Classify this cell by malaria status.
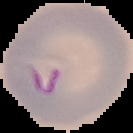

It is parasitized.

image size = 133×133 pixels
image type = cell region segmented out of the field of view; surrounding area masked to black
preparation = thin blood smear